Comment on the morphology of the erythrocytes.
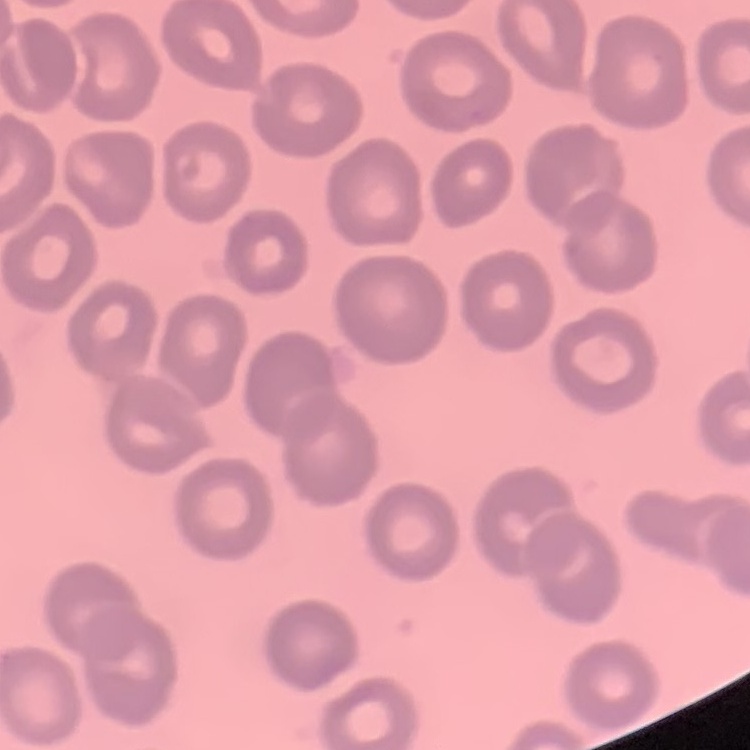

No rouleaux formation.

Thin blood smear. One tile cut from a larger photomicrograph. Stained with either Field's or Giemsa.